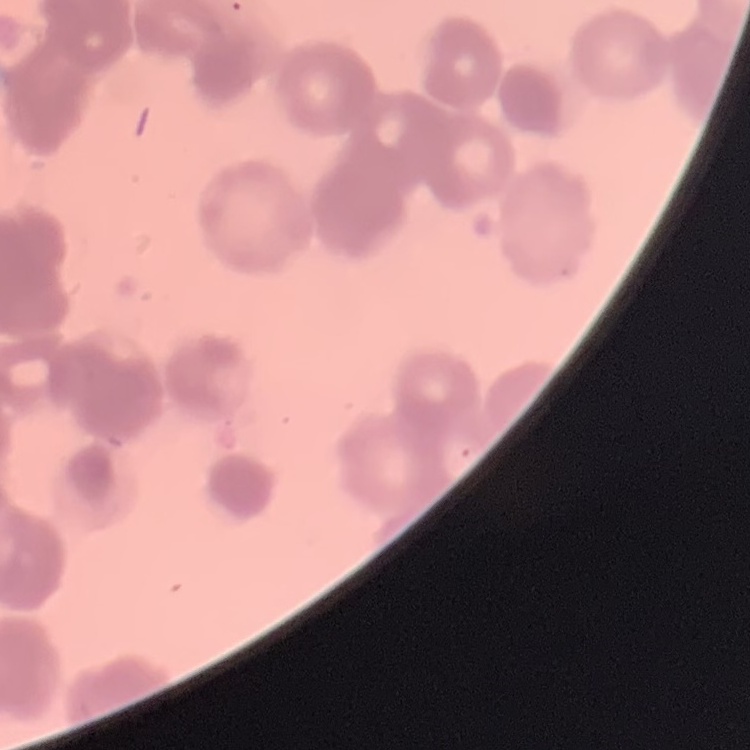

The erythrocytes show rouleaux formation. Thin blood film. Field's or Giemsa stain. One tile cut from a larger photomicrograph.